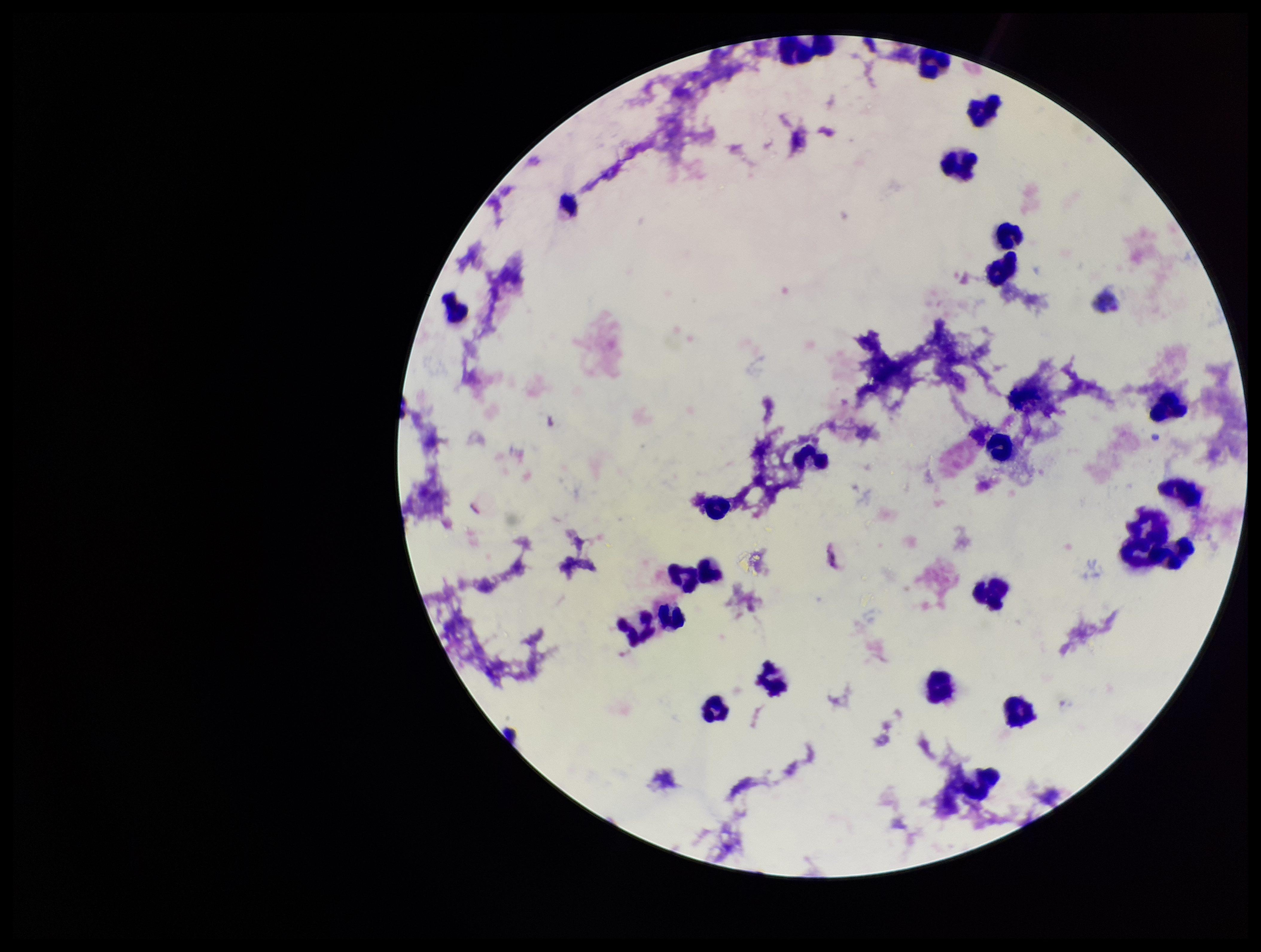
Image is 1261×952 pixels. Smartphone photograph taken through the eyepiece of a microscope. Parasite count: 0. Single field of view. Plasmodium parasites: none seen. Patient malaria status: positive. Species reported for this patient: Plasmodium vivax. Stained with Giemsa. Leukocyte count: 25. Preparation: thick smear.